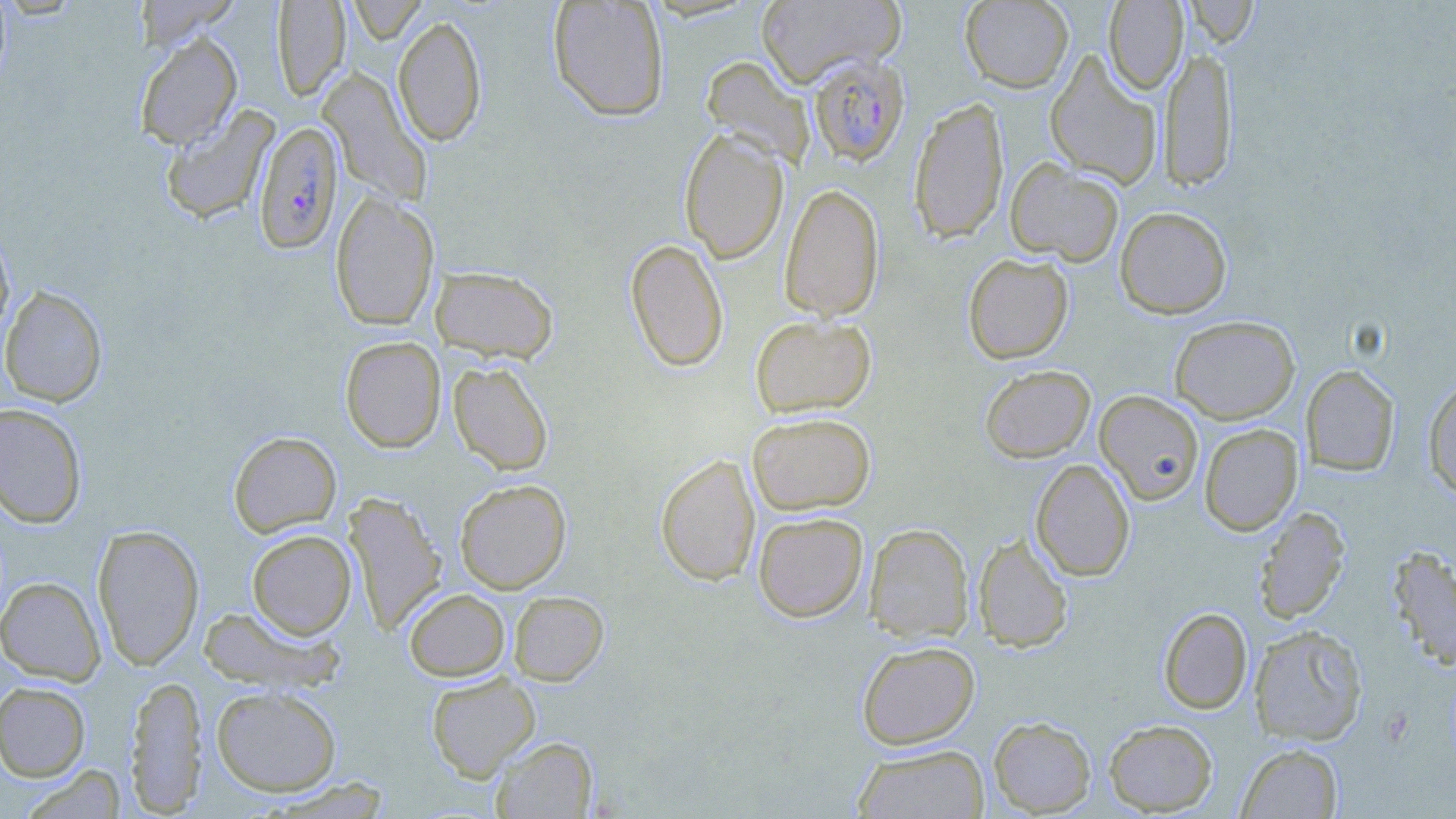
Approximate bounding boxes as (x1,y1)-(x2,y2) corner pairs in pixels. Plasmodium falciparum-infected red blood cell locations: (807,53)-(910,166), (253,121)-(344,255). Uninfected red blood cell locations: (346,0)-(428,44), (755,0)-(905,88), (960,0)-(1074,92), (1103,0)-(1187,93), (548,1)-(670,121), (1184,1)-(1258,47), (272,2)-(351,100), (393,15)-(487,146), (135,32)-(242,150), (1160,45)-(1238,191), (1045,52)-(1162,189), (701,56)-(815,168), (318,70)-(433,205), (909,97)-(1009,243), (159,105)-(280,225), (679,127)-(789,264), (1006,158)-(1125,266), (779,182)-(884,322), (330,191)-(439,332), (1115,206)-(1232,319), (0,229)-(15,341), (625,238)-(729,372), (963,253)-(1074,364), (430,266)-(558,363), (0,285)-(108,407), (750,315)-(876,418), (1170,315)-(1300,424), (340,336)-(446,453), (448,360)-(554,476), (979,365)-(1095,462), (1301,365)-(1400,476), (1423,376)-(1456,499), (1094,390)-(1204,504), (0,403)-(88,529), (747,411)-(876,515), (1199,424)-(1303,536), (228,431)-(341,537), (655,452)-(760,586), (1030,459)-(1135,581), (454,478)-(571,594), (343,491)-(448,634), (1254,506)-(1350,623), (752,511)-(868,622), (92,523)-(204,670), (864,523)-(973,643), (246,529)-(357,639), (972,533)-(1073,652), (1387,545)-(1456,671), (0,576)-(106,685), (404,588)-(510,681), (508,590)-(609,686), (197,605)-(342,692), (1158,607)-(1253,713), (1249,624)-(1368,745), (856,640)-(980,749), (426,671)-(540,782), (125,674)-(208,814), (0,681)-(91,782), (211,685)-(342,797), (988,716)-(1096,816), (1103,719)-(1219,815), (492,736)-(598,818), (1236,742)-(1343,818), (852,744)-(990,818), (19,765)-(127,818). Slide-level diagnosis: Plasmodium falciparum. Single field of view. Thin blood smear. Captured at 1000x magnification. Optical microscopy. Image is 1456×819 pixels. May-Grünwald-Giemsa-stained preparation.